Point out each malaria parasite and each leukocyte.
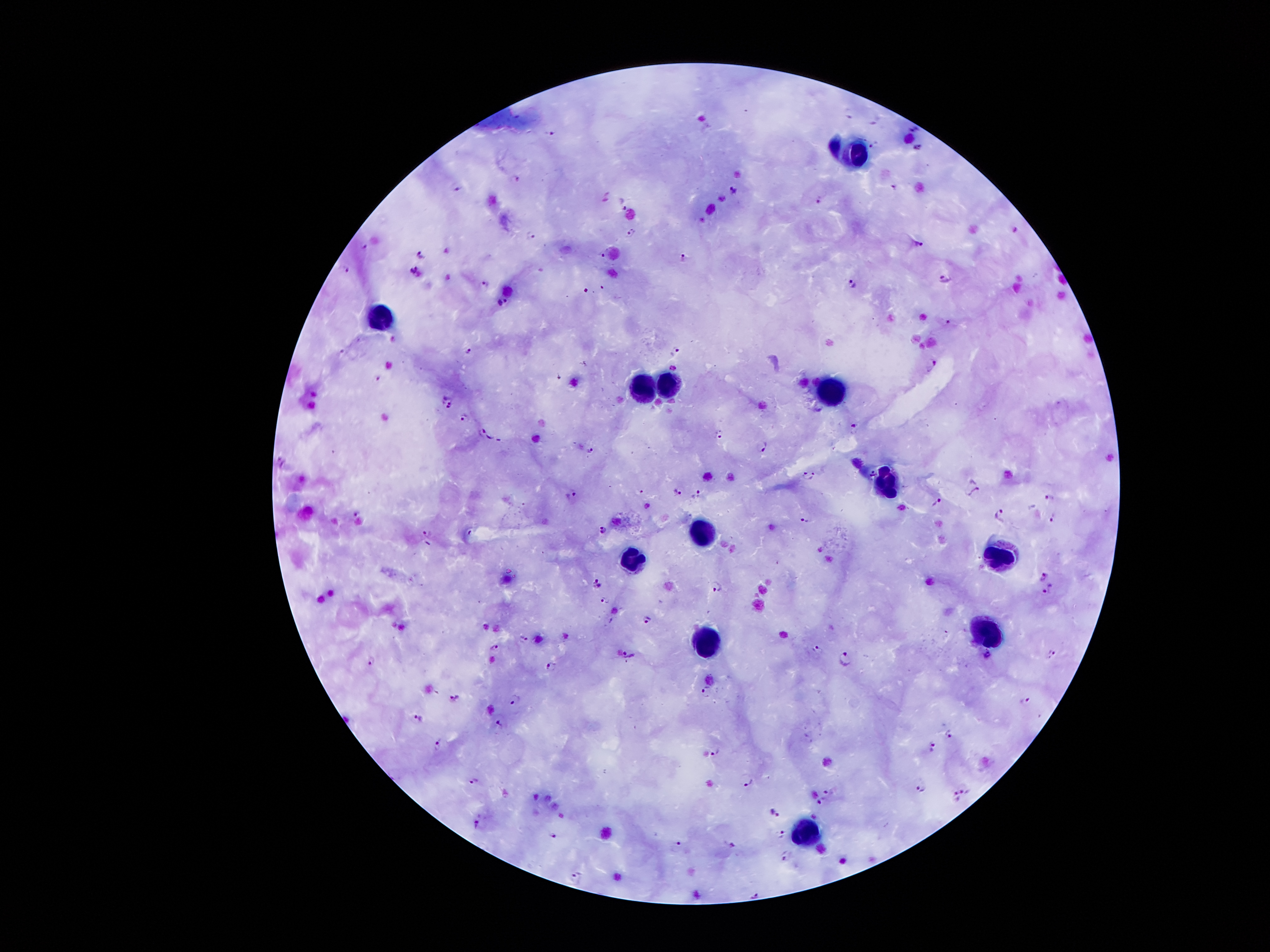

Approximate object centers, in pixels from the top-left corner.
Malaria parasites (subset; some too small to resolve): (x=916, y=131), (x=551, y=132), (x=918, y=148), (x=517, y=177), (x=458, y=186), (x=734, y=191), (x=819, y=197), (x=624, y=204), (x=1014, y=229), (x=631, y=230), (x=532, y=236), (x=920, y=242), (x=364, y=244), (x=423, y=249), (x=605, y=254), (x=685, y=255), (x=348, y=267), (x=414, y=270), (x=944, y=279), (x=851, y=282), (x=482, y=284), (x=500, y=301), (x=948, y=320), (x=469, y=348), (x=676, y=351), (x=934, y=363), (x=447, y=401), (x=465, y=417), (x=856, y=425), (x=479, y=429), (x=719, y=432), (x=763, y=444), (x=590, y=451), (x=809, y=477), (x=573, y=491), (x=974, y=491), (x=677, y=492), (x=697, y=494), (x=1049, y=495), (x=936, y=502), (x=648, y=504), (x=1001, y=513), (x=1051, y=515), (x=356, y=517), (x=804, y=520), (x=602, y=529), (x=427, y=533), (x=1044, y=574), (x=597, y=579), (x=598, y=585), (x=716, y=587), (x=1048, y=589), (x=605, y=600), (x=648, y=617), (x=522, y=638), (x=496, y=645), (x=817, y=648), (x=988, y=655), (x=629, y=656), (x=1052, y=656), (x=843, y=657), (x=370, y=660), (x=551, y=664), (x=706, y=688), (x=515, y=697), (x=452, y=700), (x=1023, y=700), (x=417, y=718), (x=499, y=723), (x=950, y=736), (x=438, y=742), (x=933, y=745), (x=716, y=752), (x=475, y=780), (x=748, y=780), (x=921, y=789), (x=965, y=789), (x=828, y=794), (x=955, y=796), (x=821, y=799), (x=774, y=811), (x=476, y=819), (x=551, y=835), (x=781, y=835), (x=678, y=844), (x=734, y=846), (x=786, y=856), (x=575, y=878), (x=754, y=895).
Leukocytes: (x=850, y=158), (x=380, y=318), (x=670, y=382), (x=641, y=384), (x=829, y=390), (x=883, y=483), (x=706, y=531), (x=1000, y=557), (x=634, y=558), (x=987, y=632), (x=710, y=642), (x=804, y=837).

capture = smartphone camera through the microscope eyepiece
magnification = 100x
stain = Giemsa
field of view = single
image size = 1270×952 pixels
preparation = thick blood film
patient malaria status = infected with Plasmodium falciparum